State which parasite is depicted.
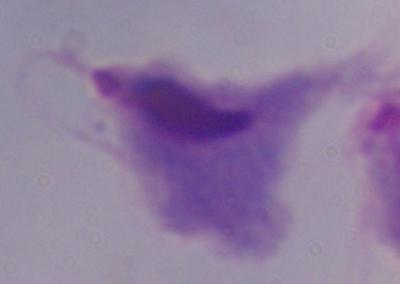
A trichomonad.

1000x magnification. Micrograph.